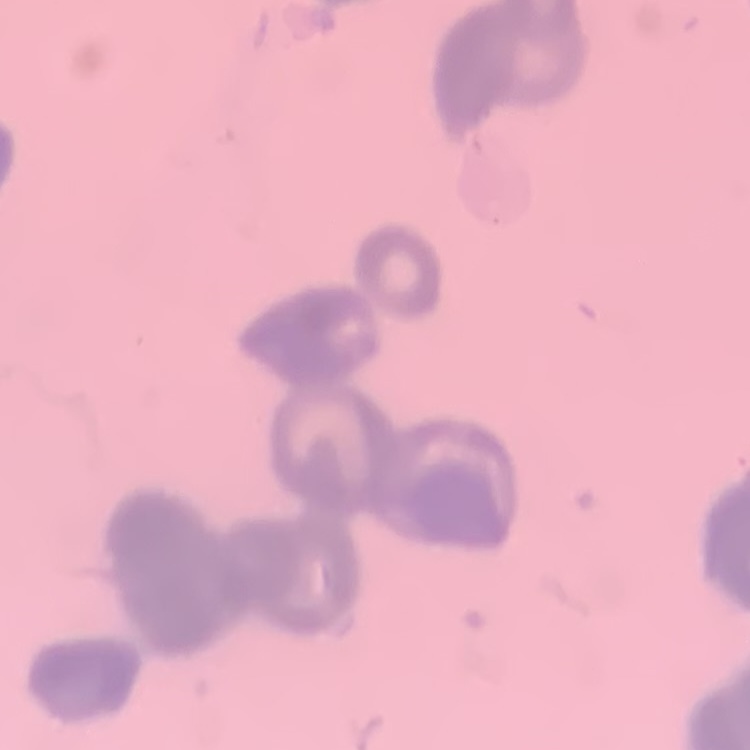
Summary:
  - Erythrocyte morphology: rouleaux formation
  - Image type: square crop of a larger photomicrograph
  - Preparation: thin peripheral smear
  - Stain: Field's or Giemsa